Identify the parasite.
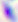

This is Toxoplasma gondii.

Summary:
  - Modality: photomicrograph
  - Magnification: 400x